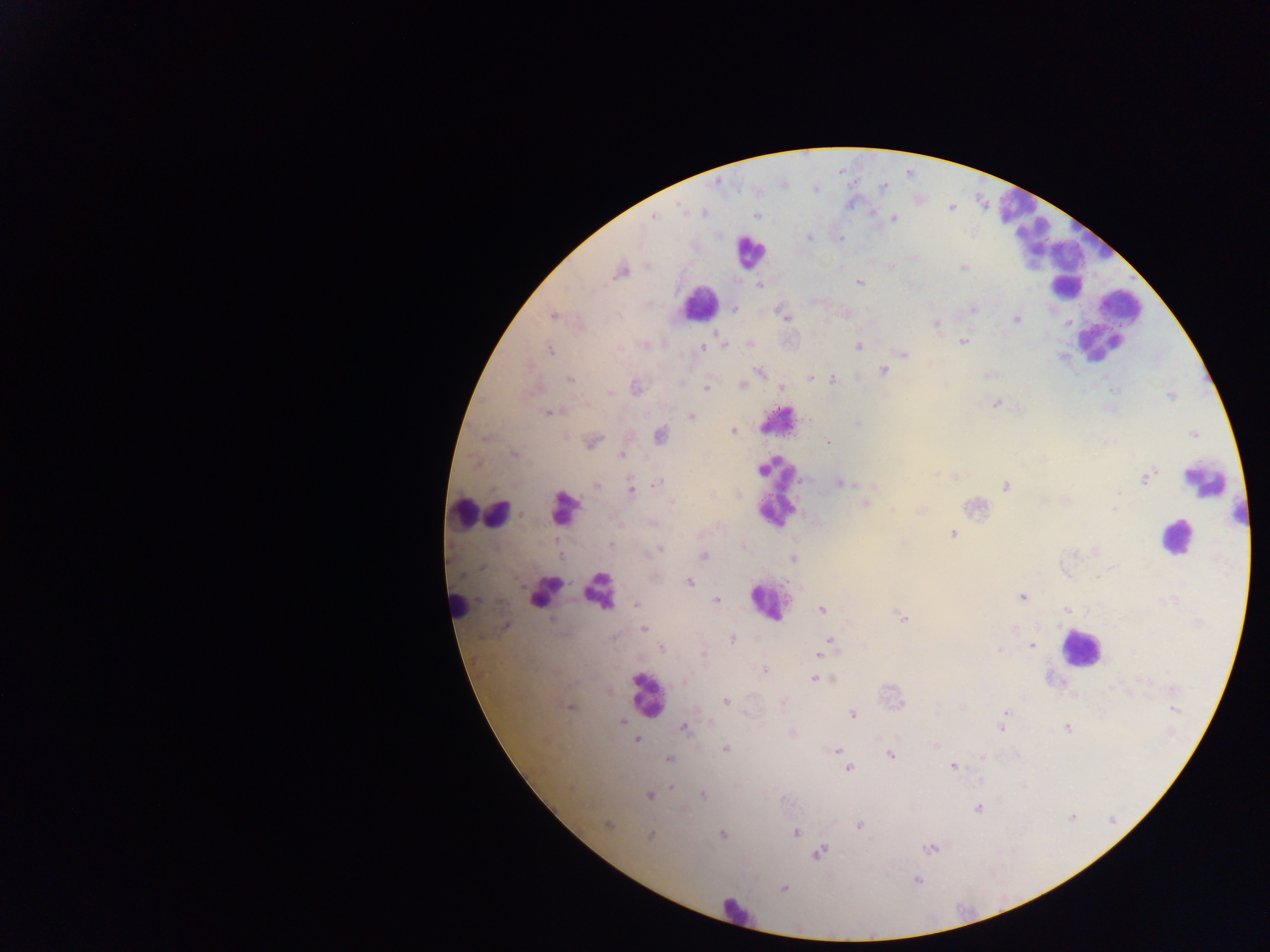
Approximate centers as (x, y) in pixels. Plasmodium parasite locations: (884, 186), (814, 188), (950, 208), (872, 212), (653, 216), (758, 216), (893, 218), (809, 236), (890, 265), (963, 267), (620, 272), (859, 281), (758, 285), (734, 309), (972, 309), (782, 311), (845, 313), (553, 315), (785, 316), (1017, 319), (936, 323), (963, 341), (749, 344), (725, 345), (701, 346), (858, 346), (548, 347), (902, 353), (883, 371), (760, 372), (988, 375), (810, 377), (570, 378), (832, 379), (741, 385), (635, 387), (705, 388), (781, 388), (609, 392), (1170, 395), (996, 404), (550, 411), (691, 416), (734, 431), (660, 434), (1194, 434), (592, 442), (826, 442), (514, 454), (621, 455), (953, 475), (1146, 477), (839, 482), (657, 483), (596, 485), (1006, 486), (630, 489), (1065, 499), (865, 502), (892, 510), (920, 510), (653, 523), (953, 534), (611, 544), (659, 549), (703, 556), (793, 559), (688, 582), (1021, 597), (716, 600), (636, 604), (821, 609), (1067, 609), (902, 616), (506, 624), (644, 629), (830, 639), (732, 640), (1032, 646), (661, 647), (824, 648), (703, 653), (819, 654), (763, 670), (814, 678), (686, 681), (725, 701), (782, 703), (569, 706), (1172, 709), (1005, 711), (852, 714), (623, 723), (709, 723), (1002, 726), (1067, 726), (683, 727), (792, 734), (637, 740), (935, 744), (725, 748), (836, 751), (890, 755), (982, 756), (668, 758), (953, 766), (848, 767), (979, 780), (671, 787), (702, 794), (649, 795), (977, 807), (1072, 816), (607, 825), (859, 825), (794, 832), (722, 834), (651, 835), (931, 847), (818, 852), (916, 880), (783, 888). Leukocyte locations: (1015, 208), (1034, 234), (1051, 246), (749, 251), (1066, 271), (1067, 286), (699, 303), (1121, 306), (1104, 334), (1099, 346), (777, 421), (1205, 480), (777, 491), (564, 508), (462, 513), (496, 513), (1239, 513), (1176, 536), (598, 590), (545, 591), (768, 600), (457, 605), (1080, 648), (647, 695), (737, 913). Thick blood smear. Mobile-phone photograph taken through the microscope. Single field of view. Sample from Ghana. Image is 1270×952 pixels.